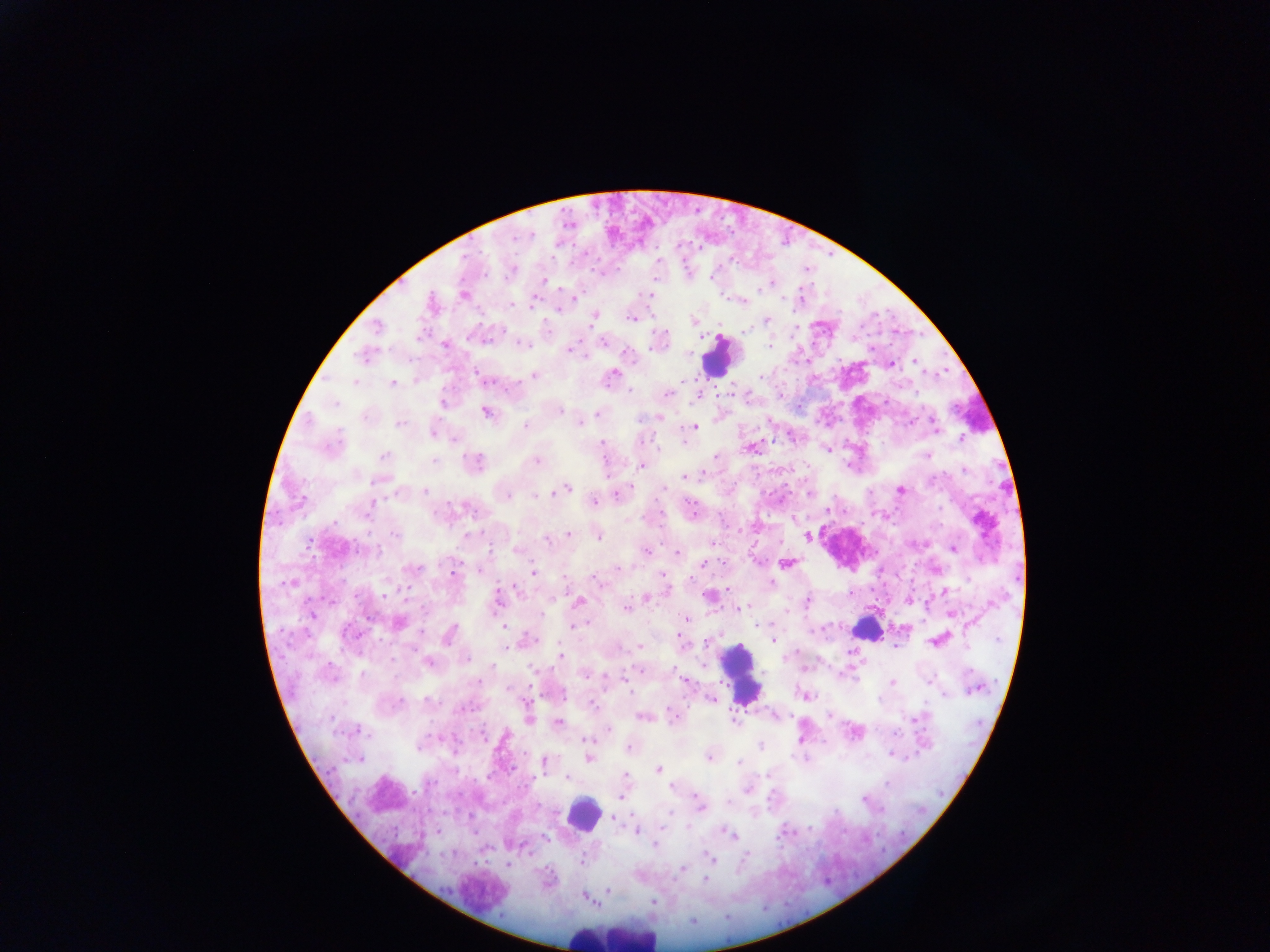
Approximate centers as x y in pixels. Leukocyte locations: 717 358; 869 625; 741 675; 583 814; 610 935. Plasmodium parasite locations: 658 260; 711 277; 544 280; 771 283; 463 294; 650 295; 575 298; 431 302; 533 303; 512 305; 558 309; 594 316; 631 319; 768 319; 693 320; 376 327; 745 330; 468 338; 487 341; 603 342; 445 344; 523 345; 770 346; 568 350; 363 356; 915 362; 891 363; 613 374; 478 375; 534 375; 761 376; 482 378; 682 380; 354 382; 392 384; 629 391; 668 394; 442 403; 335 404; 487 412; 560 412; 597 414; 641 419; 909 422; 581 423; 399 424; 935 425; 525 426; 694 427; 433 434; 962 438; 456 440; 601 443; 752 449; 827 449; 927 455; 384 456; 715 456; 434 461; 538 461; 476 462; 641 467; 965 469; 686 476; 375 482; 567 488; 664 488; 900 490; 425 491; 562 491; 552 492; 395 493; 809 493; 543 495; 617 495; 508 497; 535 497; 593 502; 371 505; 690 507; 940 507; 435 513; 367 515; 981 520; 334 523; 569 533; 395 534; 468 535; 807 536; 598 537; 547 539; 309 542; 712 543; 491 549; 954 549; 358 550; 517 550; 646 550; 376 551; 678 553; 785 563; 703 564; 415 569; 617 569; 479 571; 452 572; 534 572; 662 574; 596 579; 771 583; 287 584; 517 589; 728 590; 407 591; 944 592; 386 595; 645 597; 498 600; 579 601; 808 601; 992 602; 739 608; 626 609; 785 611; 311 614; 541 614; 952 614; 686 618; 398 622; 759 625; 504 626; 573 626; 421 632; 450 634; 531 639; 774 640; 998 640; 706 642; 937 642; 640 646; 506 648; 560 657; 783 658; 466 659; 429 663; 533 669; 639 670; 674 670; 362 673; 584 675; 684 680; 930 680; 892 682; 975 688; 508 690; 629 691; 564 695; 804 695; 944 695; 710 699; 879 699; 429 701; 401 702; 593 705; 775 716; 829 716; 643 717; 673 717; 529 718; 734 720; 915 720; 558 723; 358 730; 608 730; 483 735; 587 738; 760 745; 419 747; 629 748; 893 755; 709 758; 360 759; 589 759; 544 763; 739 763; 659 769; 625 775; 568 778; 887 784; 672 787; 748 790; 621 797; 863 799; 729 802; 700 807; 614 818; 687 826; 636 829; 724 831; 731 835; 546 838; 655 846; 529 852; 709 857; 583 862; 508 865; 682 869; 705 879; 608 890; 654 901. Mobile-phone photograph taken through the microscope. Image is 1270×952 pixels. One field of view. Thick blood film. Collected in Ghana.